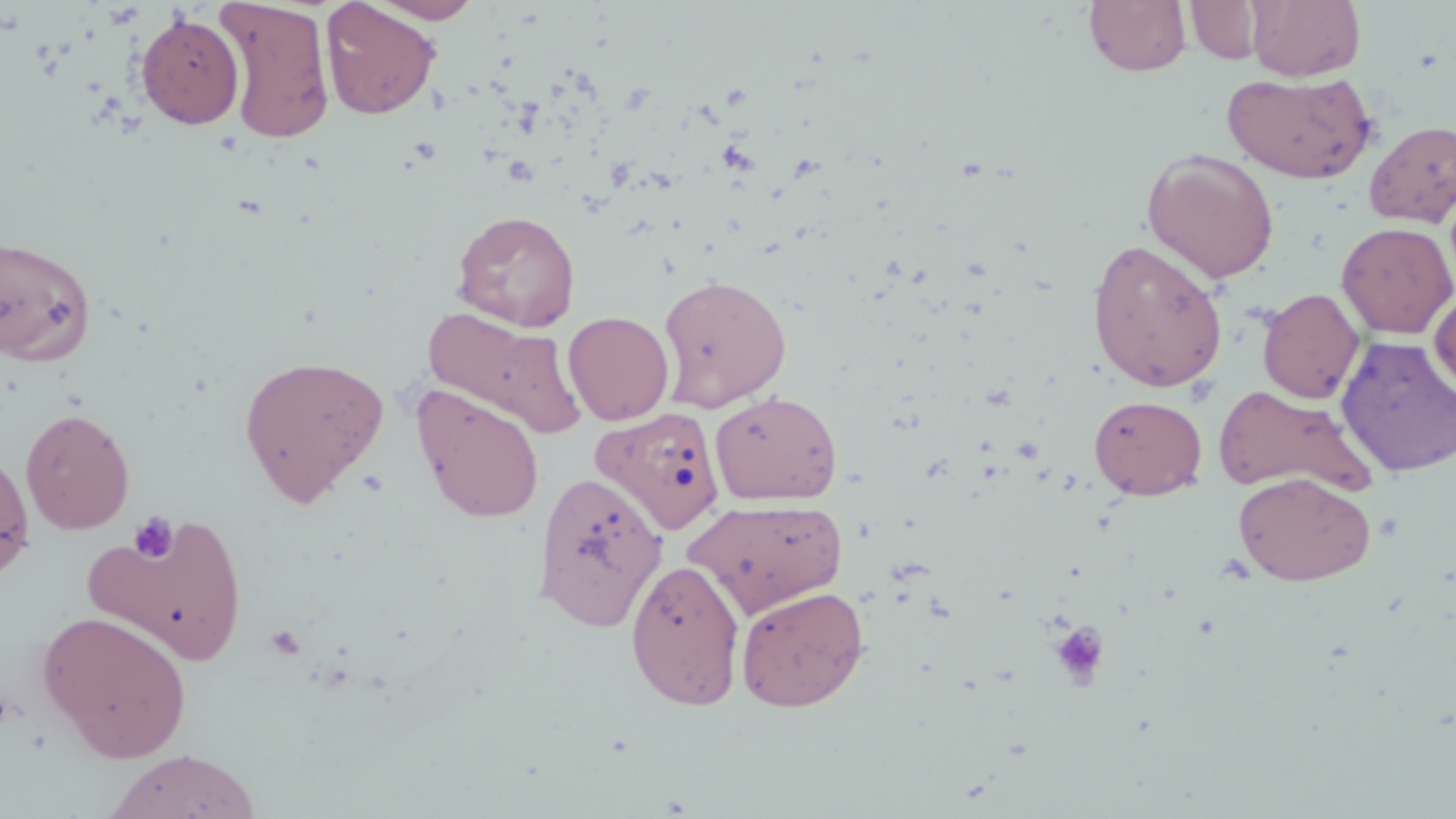

slide-level diagnosis = no evidence of blood parasites
magnification = 1000x
image size = 1456×819 pixels
uninfected red blood cell locations = approximate bounding boxes as named x1/y1/x2/y2 corners in pixels: (x1=217, y1=0, x2=335, y2=143), (x1=369, y1=0, x2=484, y2=23), (x1=1084, y1=0, x2=1191, y2=76), (x1=1247, y1=0, x2=1365, y2=81), (x1=320, y1=1, x2=441, y2=120), (x1=1186, y1=1, x2=1264, y2=64), (x1=135, y1=11, x2=244, y2=129), (x1=1221, y1=71, x2=1377, y2=184), (x1=1364, y1=120, x2=1456, y2=228), (x1=1142, y1=148, x2=1280, y2=283), (x1=452, y1=209, x2=581, y2=331), (x1=1336, y1=222, x2=1455, y2=339), (x1=0, y1=232, x2=97, y2=366), (x1=1087, y1=238, x2=1228, y2=392), (x1=657, y1=274, x2=792, y2=411), (x1=1429, y1=286, x2=1456, y2=400), (x1=1258, y1=288, x2=1365, y2=404), (x1=423, y1=307, x2=586, y2=440), (x1=563, y1=310, x2=674, y2=425), (x1=1335, y1=335, x2=1456, y2=478), (x1=238, y1=354, x2=389, y2=505), (x1=1213, y1=384, x2=1376, y2=497), (x1=412, y1=387, x2=545, y2=522), (x1=710, y1=390, x2=843, y2=505), (x1=1089, y1=395, x2=1208, y2=500), (x1=592, y1=406, x2=726, y2=536), (x1=20, y1=407, x2=135, y2=534), (x1=0, y1=445, x2=35, y2=583), (x1=1233, y1=471, x2=1376, y2=586), (x1=536, y1=472, x2=671, y2=634), (x1=684, y1=497, x2=849, y2=617), (x1=84, y1=513, x2=251, y2=666), (x1=625, y1=558, x2=746, y2=711), (x1=736, y1=585, x2=869, y2=711), (x1=37, y1=611, x2=192, y2=762), (x1=103, y1=749, x2=261, y2=819)
field of view = single
preparation = thin blood film
modality = optical microscopy
stain = May-Grünwald-Giemsa
platelet locations = approximate bounding boxes as named x1/y1/x2/y2 corners in pixels: (x1=128, y1=512, x2=179, y2=564), (x1=1049, y1=619, x2=1113, y2=690), (x1=263, y1=624, x2=307, y2=661)